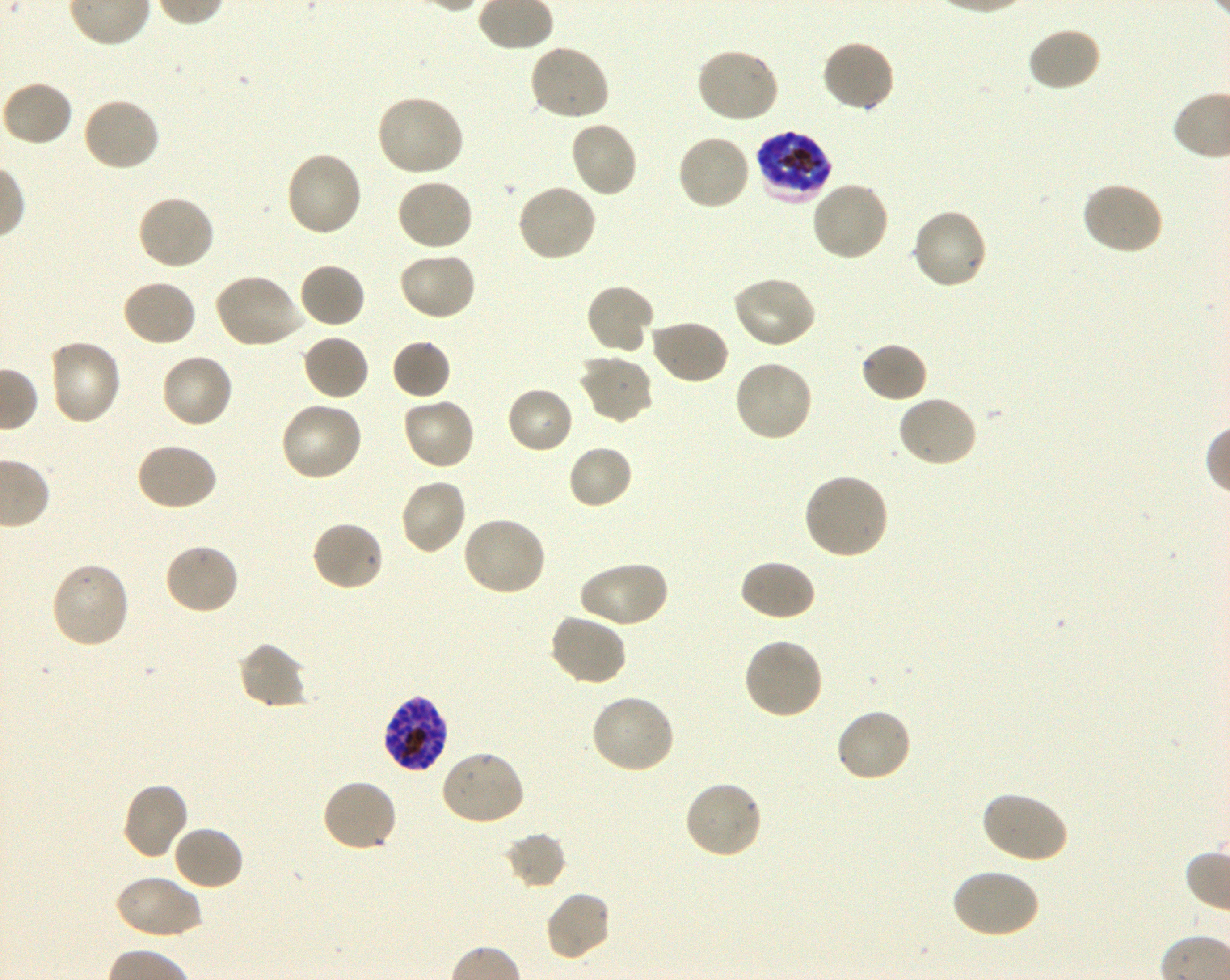
Not every red blood cell is marked. A life-cycle stage — or a range of stages, where the recorded stages span more than one — follows each staged infected red blood cell.
objective = 100x, oil immersion, numerical aperture 1.30
image size = 1230×980 pixels
donor blood group = O+
field of view = single
stain = Giemsa
locations of uninfected red blood cells = approximate bounding boxes as (x1, y1, x2, y2) in pixels: (1026, 26, 1101, 93), (820, 38, 897, 114), (527, 44, 612, 122), (696, 46, 781, 123), (1, 79, 74, 148), (375, 93, 465, 178), (82, 96, 162, 173), (569, 120, 639, 199), (676, 132, 752, 211), (285, 150, 364, 239), (396, 178, 476, 252), (809, 179, 890, 262), (1079, 181, 1164, 257), (515, 182, 598, 263), (136, 193, 216, 271), (910, 208, 989, 291), (396, 251, 477, 322), (297, 262, 366, 329), (213, 272, 305, 349), (731, 275, 818, 350), (121, 279, 198, 348), (585, 282, 655, 356), (649, 318, 730, 385), (301, 334, 371, 402), (46, 338, 122, 427), (391, 339, 451, 400), (859, 341, 929, 404), (160, 352, 235, 430), (577, 353, 653, 424), (733, 359, 814, 443), (505, 386, 575, 455), (895, 395, 978, 469), (401, 396, 476, 471), (279, 400, 364, 482), (134, 442, 219, 511), (567, 444, 634, 510), (802, 472, 890, 560), (399, 477, 468, 555), (460, 515, 547, 597), (311, 519, 385, 591), (162, 542, 240, 617), (738, 558, 817, 622), (578, 559, 669, 629), (49, 561, 132, 650), (548, 612, 628, 688), (742, 637, 825, 720), (236, 641, 308, 710), (588, 694, 676, 775), (834, 707, 914, 784), (440, 749, 526, 827), (320, 778, 398, 853), (682, 778, 764, 860), (120, 780, 190, 861), (979, 790, 1069, 864), (172, 824, 245, 891), (503, 832, 566, 889), (949, 868, 1040, 940), (115, 874, 202, 940), (543, 890, 611, 963)
culture = in-vitro Plasmodium falciparum strain 3D7, shaking
preparation = thin blood film
locations of infected red blood cells = approximate bounding boxes as (x1, y1, x2, y2) in pixels: (754, 129, 834, 203) late trophozoite to late schizont; (381, 693, 450, 772) schizont